Assess this cell for malaria.
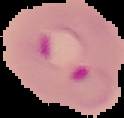

Parasitized.

Summary:
  - Image type: cell region segmented out of the field of view; surrounding area masked to black
  - Preparation: thin blood smear
  - Image size: 124×118 pixels